Classify this cell by malaria status.
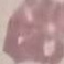
Uninfected.

Summary:
  - Preparation: thin smear
  - Capture: smartphone through the microscope eyepiece
  - Stain: Giemsa
  - Image type: automatically extracted cell patch, resized to 64 × 64 pixels